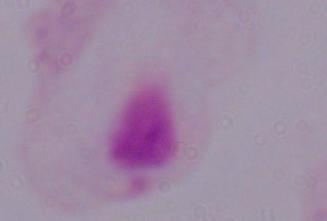

{
  "modality": "micrograph",
  "magnification": "1000x",
  "identification": "trichomonad"
}